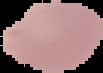
Summary:
  - Image size: 103×73 pixels
  - Malaria status: uninfected
  - Preparation: thin blood film
  - Image type: segmented cell region on a black background